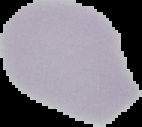
Summary:
  - Image type: cell region segmented out of the field of view; surrounding area masked to black
  - Preparation: thin blood film
  - Result: negative for malaria parasites
  - Image size: 142×127 pixels